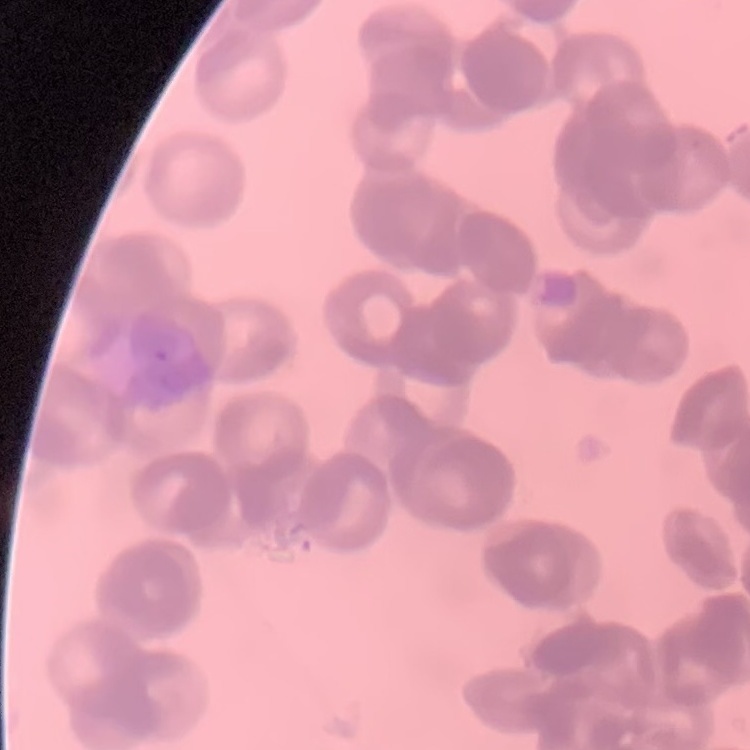
red_blood_cell_morphology: rouleaux formation
preparation: thin blood film
stain: Field's or Giemsa
image_type: one tile cut from a larger photomicrograph